Identify the parasite.
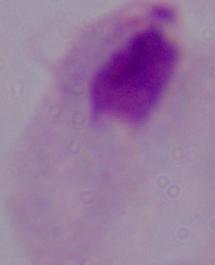
This is a trichomonad.

Captured at 1000x magnification. Micrograph.